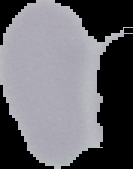

Summary:
  - Malaria status: uninfected
  - Image size: 133×169 pixels
  - Image type: cell region segmented out of the field of view; surrounding area masked to black
  - Preparation: thin blood smear